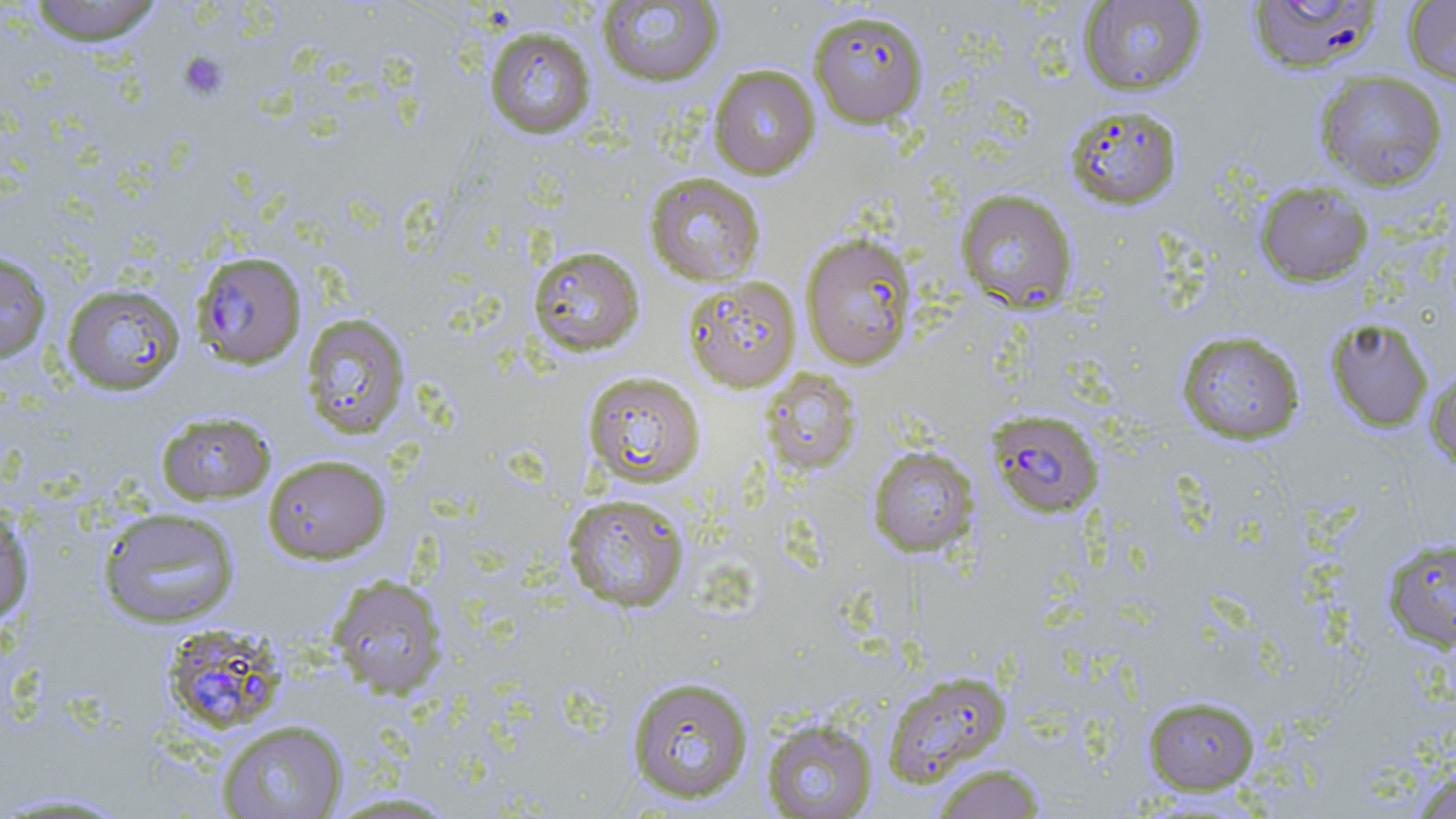
Approximate bounding boxes as [x1, y1, x2, y2] in pixels. Uninfected red blood cell locations: [25, 0, 165, 46], [1246, 0, 1383, 75], [596, 1, 724, 88], [1078, 1, 1206, 95], [1403, 1, 1456, 86], [808, 8, 929, 128], [483, 26, 597, 139], [708, 65, 821, 180], [1314, 70, 1449, 191], [1063, 104, 1183, 209], [644, 173, 766, 286], [1255, 180, 1373, 287], [955, 188, 1079, 313], [800, 233, 918, 370], [527, 245, 646, 357], [0, 251, 52, 365], [682, 275, 802, 392], [60, 283, 185, 395], [299, 312, 412, 440], [1324, 317, 1434, 433], [1176, 330, 1305, 445], [1424, 360, 1456, 473], [760, 369, 862, 476], [581, 371, 706, 489], [155, 411, 276, 505], [867, 445, 979, 557], [262, 454, 391, 564], [561, 492, 691, 613], [0, 504, 35, 626], [97, 507, 241, 629], [1381, 537, 1456, 652], [326, 573, 448, 698], [882, 670, 1013, 786], [626, 674, 754, 805], [1142, 694, 1261, 794], [760, 717, 878, 818], [216, 719, 349, 819], [931, 763, 1047, 819], [1410, 766, 1456, 819], [0, 789, 137, 817], [320, 790, 465, 817]. Plasmodium falciparum-infected red blood cell locations: [191, 251, 307, 369], [986, 409, 1104, 518], [161, 623, 288, 736]. Platelet locations: [178, 52, 228, 100]. Slide-level diagnosis: Plasmodium falciparum. Optical microscopy. 1000x magnification. One field of a larger specimen. Image is 1456×819 pixels. Thin blood smear. May-Grünwald-Giemsa stain.